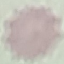

malaria status = uninfected
stain = Giemsa
preparation = thin blood film
capture = smartphone through the microscope eyepiece
image type = cell patch, automatically extracted from a larger field of view and resized to 64 × 64 pixels